Assess this cell for malaria.
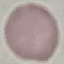

It is uninfected.

Summary:
  - Stain: Giemsa
  - Capture: smartphone through the microscope eyepiece
  - Image type: cell patch, automatically extracted from a larger field of view and resized to 64 × 64 pixels
  - Preparation: thin blood film